Report the malaria status of this cell.
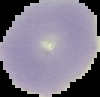
Uninfected.

Summary:
  - Preparation: thin blood smear
  - Image size: 100×97 pixels
  - Image type: segmented cell region with the area outside set to black